Name the cell type shown.
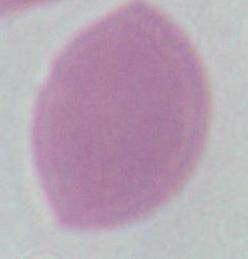
An erythrocyte.

Summary:
  - Modality: micrograph
  - Magnification: 1000x